Describe the morphology of the erythrocytes.
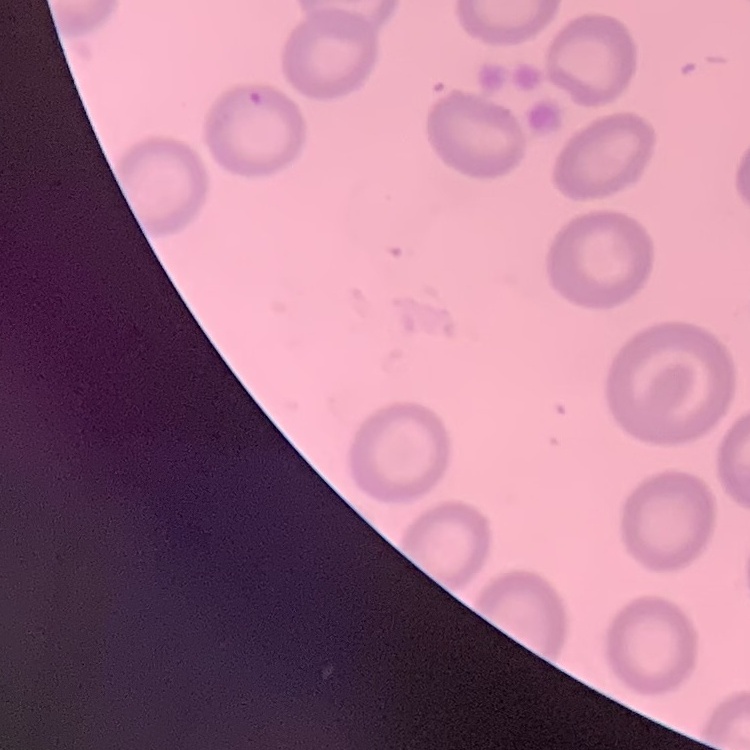
They show no rouleaux formation.

One tile cut from a larger photomicrograph. Thin blood smear. Field's or Giemsa stain.